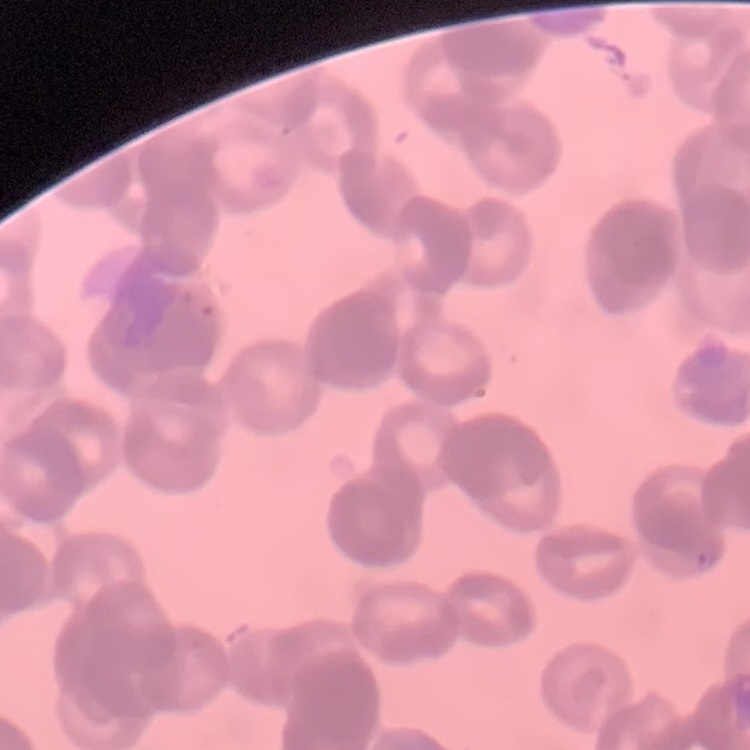

erythrocyte morphology = rouleaux formation
preparation = thin blood film
stain = Field's or Giemsa
image type = square crop of a larger photomicrograph